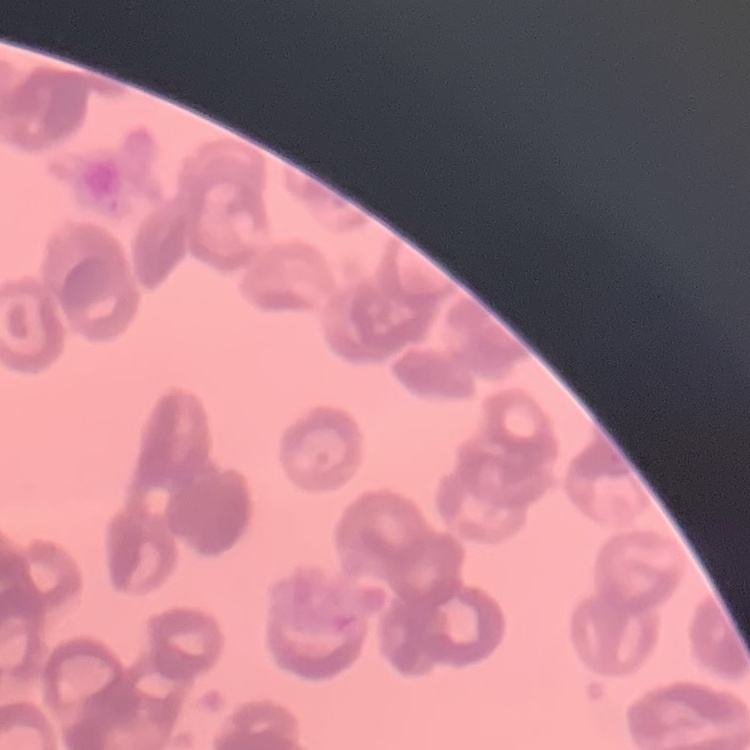

erythrocyte morphology = rouleaux formation
stain = Field's or Giemsa
preparation = thin blood film
image type = one tile cut from a larger photomicrograph